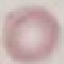

malaria status = uninfected
capture = smartphone camera at the microscope eyepiece
preparation = thin blood film
stain = Giemsa
image type = automatically extracted cell patch, resized to 64 × 64 pixels